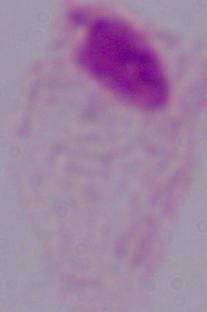

A trichomonad is seen. Captured at 1000x magnification. Photomicrograph.